Name the parasite shown.
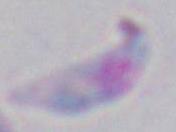

Toxoplasma gondii.

1000x magnification. Photomicrograph.